Assess the morphology of the red blood cells.
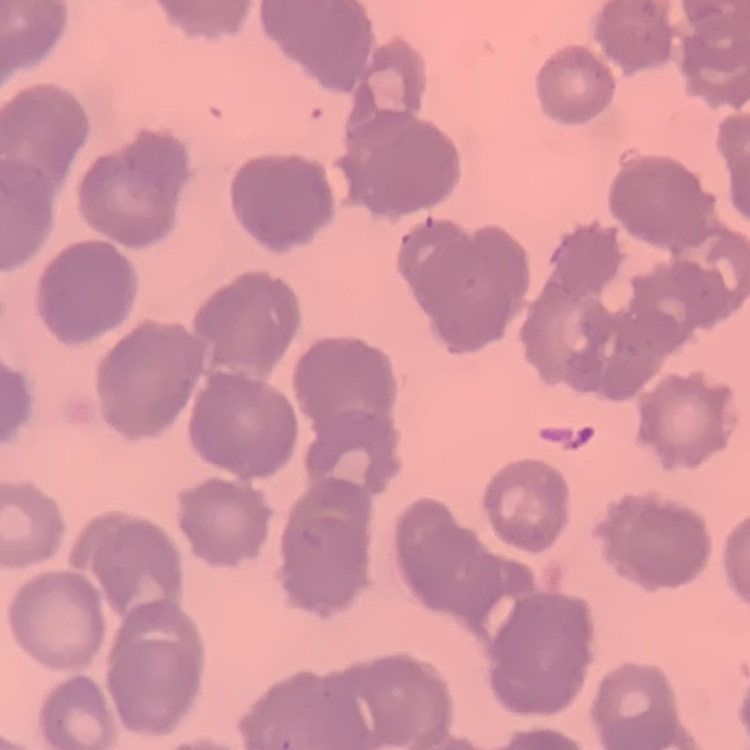

They show rouleaux formation.

Field's or Giemsa stain. Thin peripheral smear. Square crop of a larger photomicrograph.